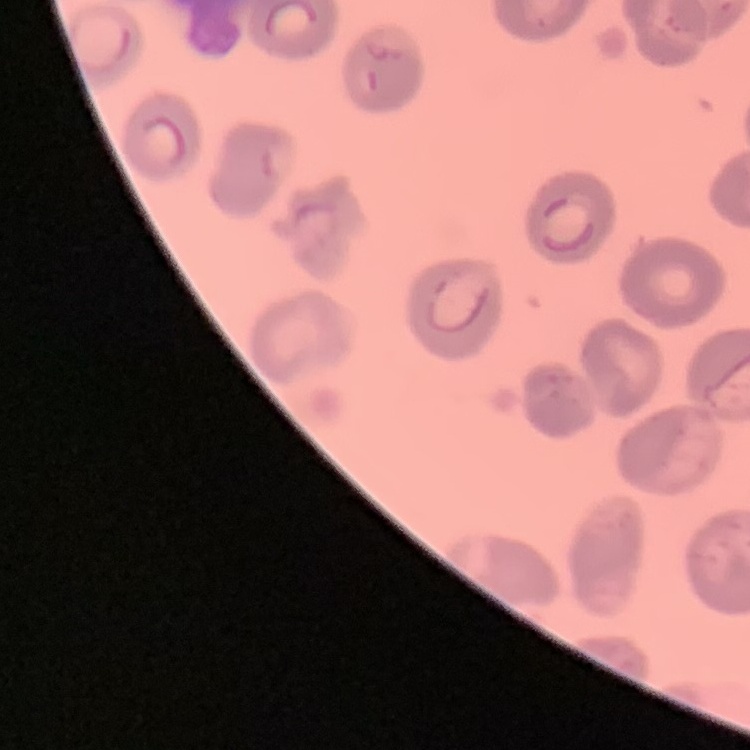

Summary:
  - Red blood cell morphology: no rouleaux formation
  - Preparation: thin blood film
  - Stain: Field's or Giemsa
  - Image type: one tile cut from a larger photomicrograph